Locate and identify every blood parasite.
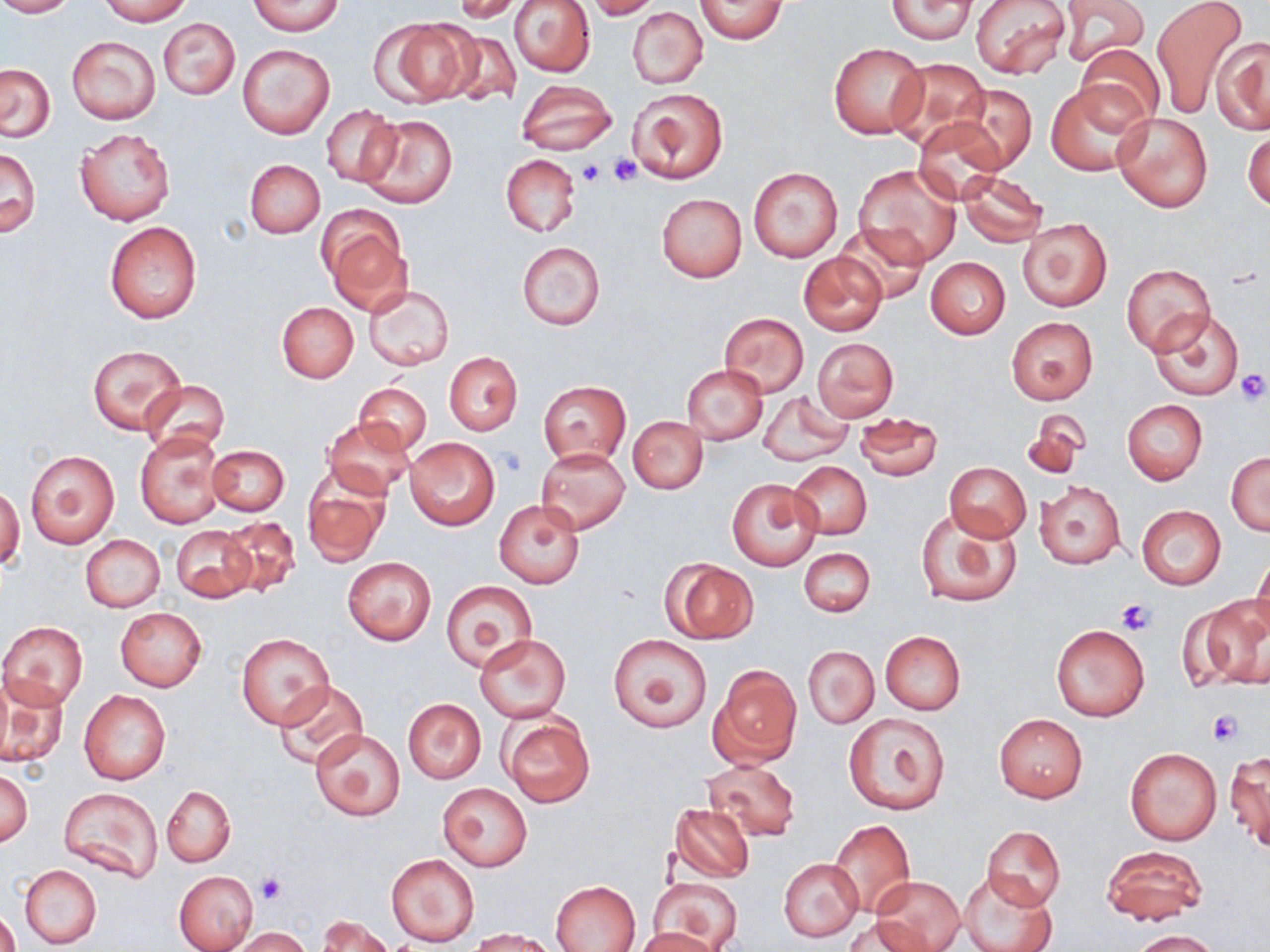

No blood parasites observed.

Summary:
  - Coordinate format: approximate bounding boxes as (x1, y1, x2, y2) in pixels
  - Platelet locations: (608, 154, 641, 186), (575, 159, 605, 185), (1234, 369, 1269, 405), (1116, 598, 1155, 636), (1207, 709, 1242, 747), (254, 872, 289, 906)
  - Uninfected red blood cell locations: (0, 0, 76, 17), (100, 0, 192, 24), (250, 0, 345, 35), (509, 0, 595, 78), (586, 0, 662, 19), (695, 0, 789, 46), (886, 0, 980, 43), (972, 0, 1071, 79), (1057, 0, 1150, 68), (1151, 0, 1250, 118), (453, 1, 524, 23), (628, 7, 707, 88), (157, 18, 240, 100), (376, 18, 476, 105), (437, 28, 523, 108), (67, 36, 160, 124), (1212, 37, 1270, 134), (828, 43, 928, 139), (238, 45, 334, 138), (1075, 45, 1164, 129), (886, 57, 992, 149), (1, 64, 55, 141), (517, 79, 618, 156), (1046, 80, 1148, 175), (947, 83, 1038, 174), (627, 88, 727, 184), (322, 105, 401, 188), (1113, 112, 1213, 212), (360, 114, 458, 208), (912, 118, 1007, 203), (1243, 124, 1270, 213), (75, 128, 175, 225), (1, 147, 42, 237), (502, 154, 580, 236), (245, 159, 325, 238), (854, 164, 962, 266), (749, 166, 843, 263), (955, 168, 1047, 247), (657, 193, 746, 282), (320, 212, 410, 311), (1018, 217, 1112, 312), (105, 221, 201, 324), (836, 223, 929, 305), (517, 242, 606, 329), (798, 251, 888, 338), (925, 256, 1011, 339), (1120, 262, 1217, 354), (363, 285, 455, 372), (276, 302, 358, 383), (1147, 309, 1247, 401), (718, 312, 808, 399), (1005, 316, 1098, 405), (813, 338, 898, 422), (87, 343, 185, 436), (444, 352, 523, 436), (684, 366, 768, 444), (142, 379, 229, 455), (539, 380, 631, 465), (355, 382, 433, 455), (758, 391, 852, 467), (1122, 399, 1207, 484), (1021, 408, 1091, 480), (853, 412, 944, 481), (324, 416, 417, 499), (628, 416, 707, 494), (135, 431, 225, 528), (404, 435, 501, 530), (208, 445, 289, 516), (536, 448, 630, 533), (26, 450, 119, 548), (1227, 452, 1269, 535), (789, 461, 871, 539), (944, 462, 1031, 542), (302, 464, 391, 568), (727, 479, 822, 571), (1035, 481, 1125, 569), (0, 484, 24, 571), (494, 500, 585, 588), (1136, 504, 1226, 590), (916, 510, 1023, 609), (217, 516, 300, 599), (169, 525, 257, 602), (81, 535, 164, 612), (799, 548, 875, 617), (1252, 552, 1270, 641), (342, 558, 436, 645), (664, 559, 758, 643), (441, 580, 536, 671), (1189, 599, 1270, 693), (115, 607, 207, 691), (1, 622, 88, 710), (1050, 623, 1149, 722), (880, 630, 966, 715), (237, 633, 334, 727), (474, 633, 571, 724), (606, 634, 711, 733), (803, 646, 879, 728), (708, 663, 801, 769), (1, 677, 69, 770), (274, 680, 368, 769), (79, 689, 171, 785), (403, 698, 486, 783), (843, 712, 951, 815), (993, 713, 1089, 802), (501, 714, 595, 807), (311, 729, 406, 820), (1125, 746, 1222, 846), (1226, 751, 1269, 853), (703, 758, 801, 842), (0, 768, 32, 847), (439, 783, 532, 870), (60, 786, 161, 884), (161, 786, 235, 866), (670, 802, 755, 883), (828, 819, 915, 916), (981, 825, 1066, 912), (1101, 845, 1206, 926), (386, 853, 480, 947), (780, 858, 863, 941), (19, 865, 102, 949), (173, 871, 259, 952), (960, 871, 1058, 952), (869, 876, 965, 952), (647, 877, 742, 952), (551, 880, 641, 951), (0, 910, 20, 952), (317, 915, 393, 952), (847, 918, 931, 950), (230, 928, 313, 952), (469, 928, 560, 952), (633, 928, 723, 952), (1133, 930, 1220, 951)
  - Slide-level diagnosis: negative for blood parasites
  - Image size: 1270×952 pixels
  - Magnification: 1000x
  - Modality: light microscopy
  - Preparation: thin blood smear
  - Field of view: single
  - Stain: May-Grünwald-Giemsa